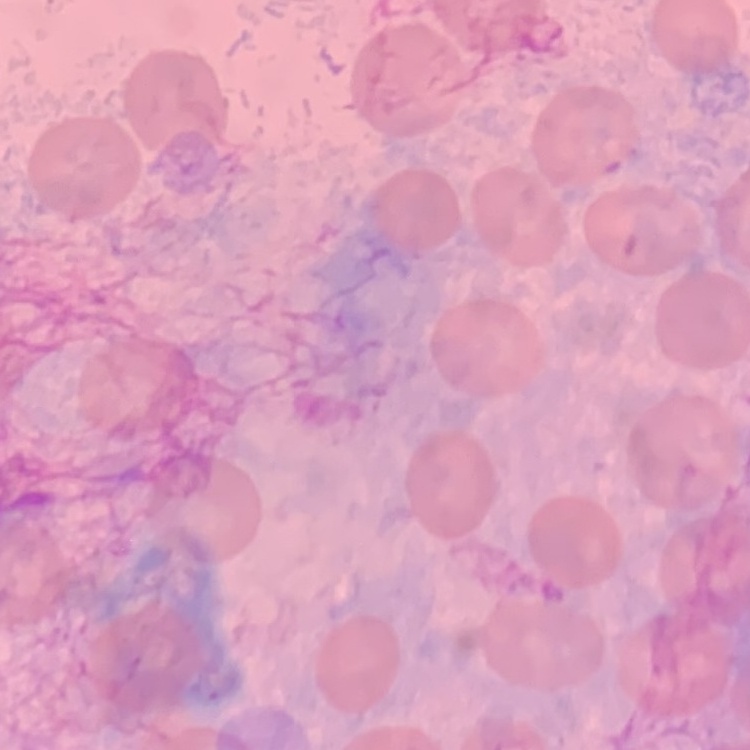

The erythrocytes show no rouleaux formation. Stained with either Field's or Giemsa. Thin peripheral smear. One tile cut from a larger photomicrograph.